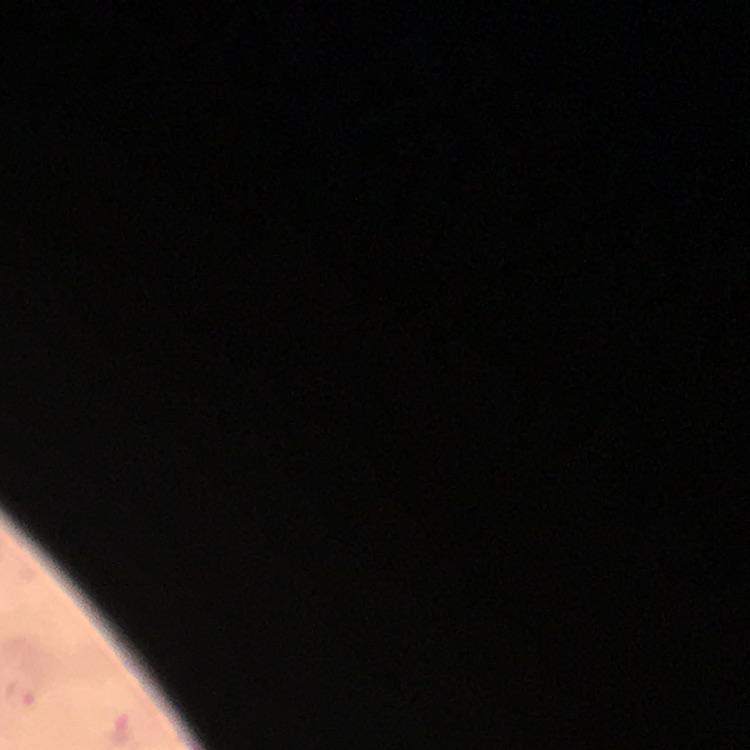
{
  "capture": "smartphone photograph through a microscope",
  "stain": "Giemsa",
  "magnification": "100x",
  "preparation": "thick blood film",
  "context": "from a malaria diagnostic workup",
  "immersion_oil": "used",
  "cropped_from": "one field of view",
  "malaria_parasite_locations": "approximate centers as [x, y] in pixels: [20, 693], [121, 730]",
  "image_size": "750×750 pixels"
}